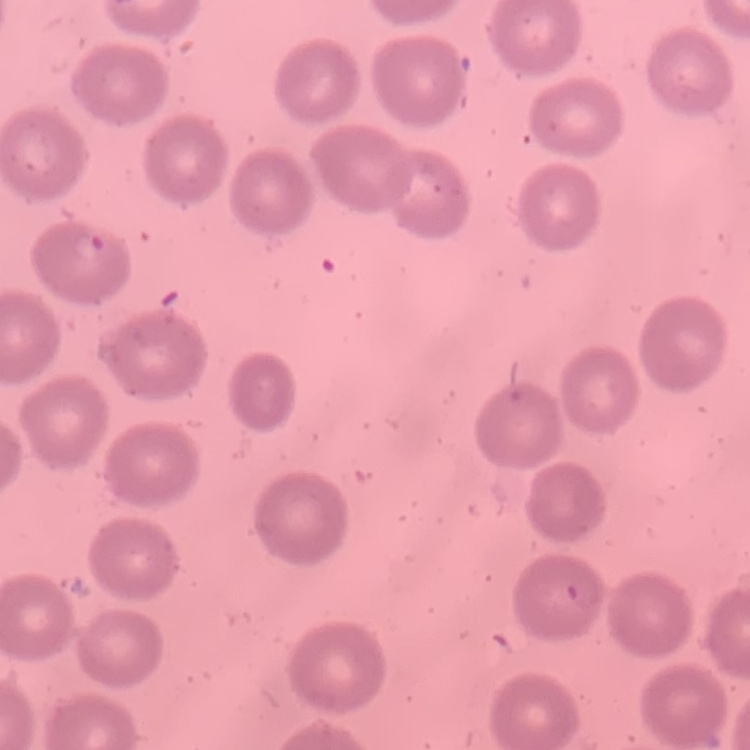

red blood cell morphology = no rouleaux formation
stain = Field's or Giemsa
preparation = thin peripheral smear
image type = square crop of a larger photomicrograph